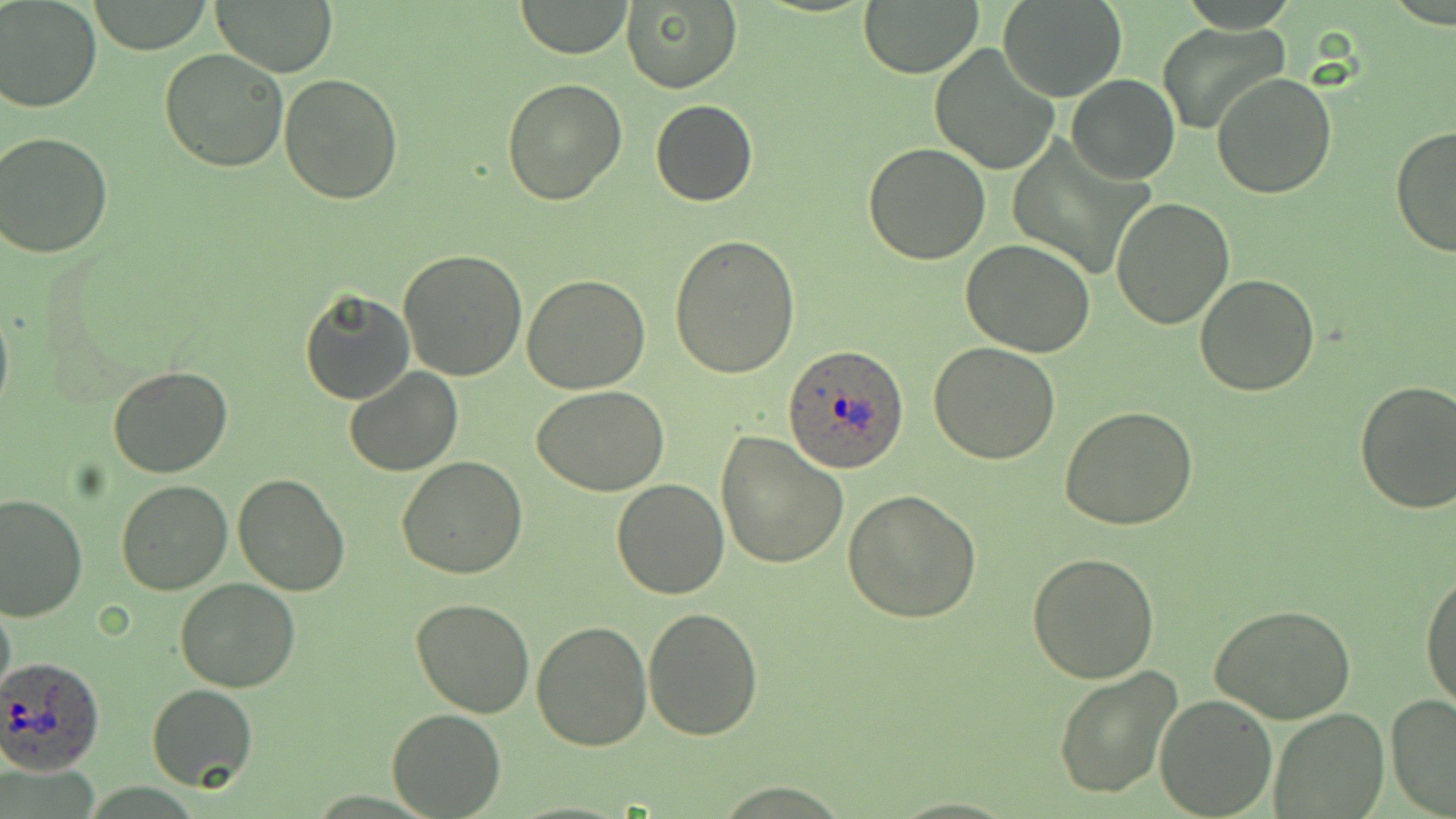

Summary:
  - Coordinate format: approximate bounding boxes as (x1, y1, x2, y2) in pixels
  - Uninfected red blood cell locations: (1, 0, 101, 112), (87, 0, 216, 53), (210, 0, 340, 76), (510, 1, 633, 57), (859, 1, 981, 76), (998, 1, 1127, 101), (620, 3, 741, 92), (1158, 23, 1287, 134), (929, 42, 1060, 175), (159, 48, 290, 172), (1211, 72, 1338, 198), (279, 74, 404, 206), (1067, 74, 1180, 184), (501, 77, 629, 206), (649, 98, 758, 207), (1389, 124, 1456, 259), (1, 130, 116, 259), (863, 143, 991, 264), (1111, 195, 1236, 330), (670, 234, 801, 378), (961, 237, 1096, 357), (398, 246, 528, 381), (522, 274, 652, 393), (1194, 274, 1319, 396), (300, 288, 414, 404), (0, 298, 13, 423), (928, 343, 1059, 463), (108, 363, 234, 479), (344, 367, 462, 477), (1354, 380, 1456, 515), (531, 386, 670, 496), (1059, 406, 1200, 532), (716, 431, 848, 570), (397, 455, 529, 580), (231, 473, 350, 595), (610, 479, 730, 599), (116, 480, 233, 595), (844, 489, 982, 624), (0, 494, 87, 624), (1027, 553, 1160, 683), (1420, 567, 1456, 713), (176, 578, 302, 693), (0, 591, 16, 705), (409, 598, 537, 718), (1210, 603, 1358, 725), (643, 607, 763, 740), (532, 622, 651, 751), (1054, 664, 1185, 800), (145, 684, 257, 791), (1385, 693, 1456, 818), (1153, 694, 1277, 818), (387, 706, 505, 818), (1270, 707, 1387, 818)
  - Plasmodium ovale-infected red blood cell locations: (783, 345, 909, 472), (0, 655, 105, 776)
  - Slide-level diagnosis: Plasmodium ovale
  - Magnification: 1000x
  - Image size: 1456×819 pixels
  - Modality: optical microscopy
  - Preparation: thin blood film
  - Field of view: single
  - Stain: May-Grünwald-Giemsa